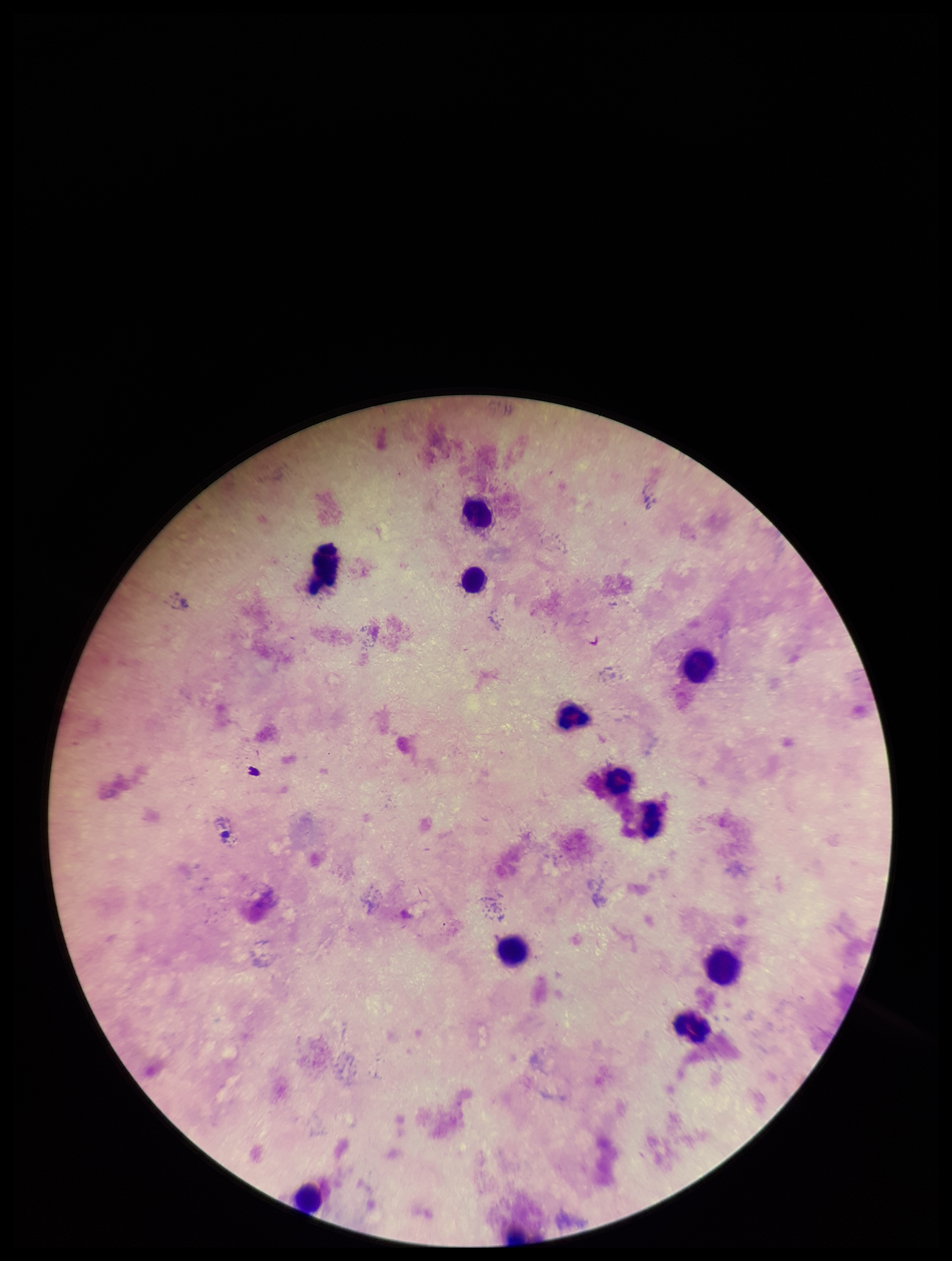
Summary:
  - Capture: smartphone photograph through the microscope eyepiece
  - Patient malaria status: negative
  - Stain: Giemsa
  - Leukocyte count: 11
  - Plasmodium parasites: none seen
  - Preparation: thick blood smear
  - Image size: 952×1261 pixels
  - Field of view: one from this slide
  - Parasite count: 0